Identify the blood parasite species.
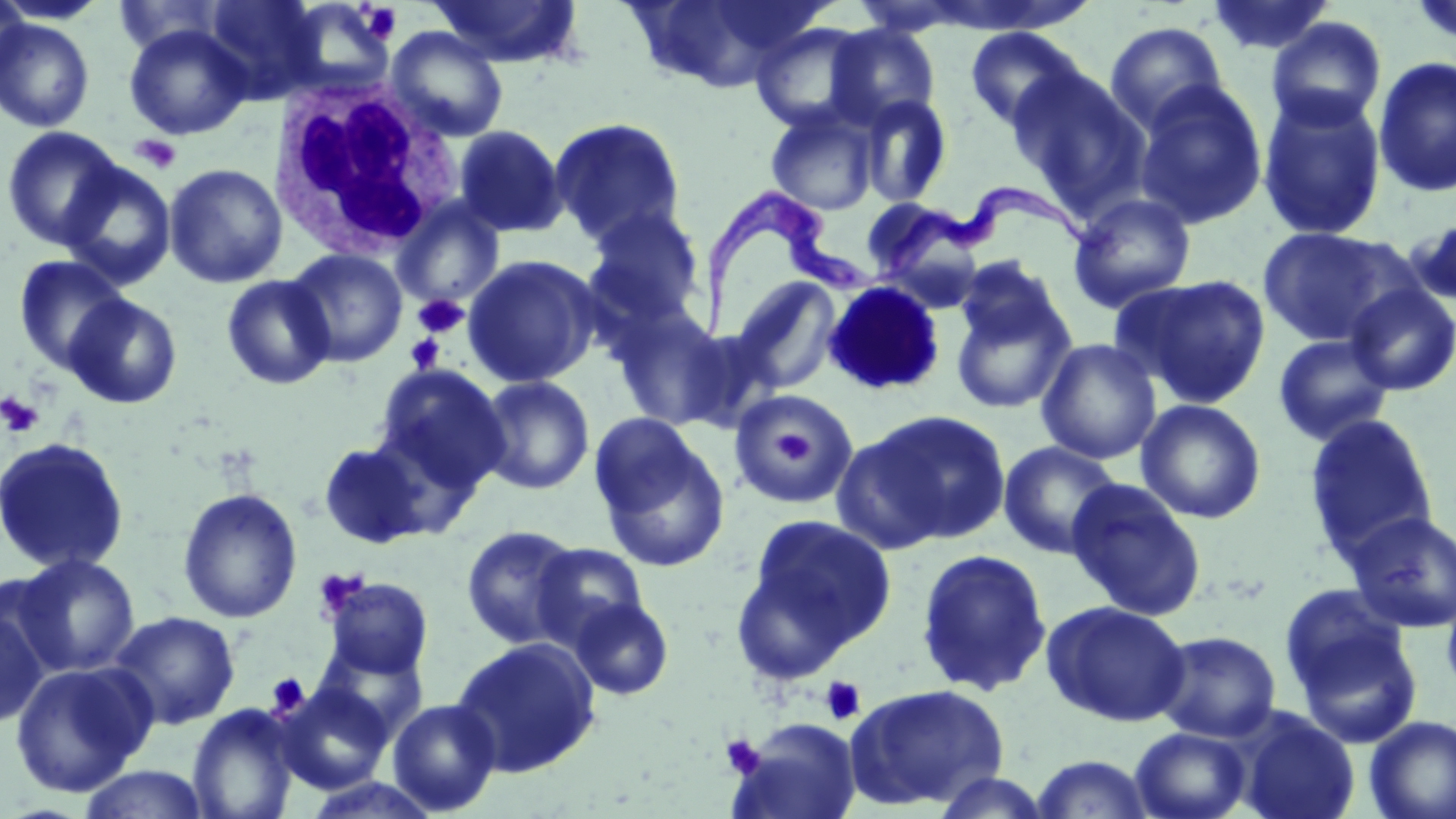

Trypanosoma brucei.

platelet_locations: 'approximate bounding boxes as [x1, y1, x2, y2] in pixels: [360, 3, 403, 44], [130, 134, 182, 174], [413, 294, 468, 338], [404, 333, 446, 375], [0, 391, 45, 438], [763, 414, 827, 479], [266, 673, 309, 716], [820, 676, 866, 726], [721, 734, 765, 778]'
uninfected_red_blood_cell_locations: 'approximate bounding boxes as [x1, y1, x2, y2] in pixels: [0, 0, 30, 90], [0, 0, 110, 26], [114, 0, 228, 58], [203, 0, 326, 102], [429, 0, 584, 68], [1206, 0, 1336, 57], [1408, 0, 1456, 51], [631, 1, 822, 92], [1266, 17, 1387, 132], [0, 18, 95, 133], [749, 21, 875, 133], [1105, 21, 1228, 135], [824, 23, 941, 128], [124, 24, 253, 140], [964, 25, 1090, 132], [386, 26, 510, 143], [1373, 56, 1456, 198], [1006, 66, 1150, 212], [1133, 81, 1269, 229], [857, 93, 953, 208], [1257, 93, 1387, 242], [765, 105, 879, 216], [548, 117, 687, 248], [452, 124, 568, 239], [1, 126, 127, 251], [58, 160, 177, 289], [163, 163, 288, 289], [1067, 192, 1197, 313], [859, 197, 983, 287], [392, 198, 505, 309], [581, 206, 707, 329], [1407, 217, 1456, 306], [1255, 225, 1412, 347], [285, 248, 408, 368], [13, 254, 131, 373], [462, 254, 603, 388], [954, 255, 1068, 357], [1116, 273, 1273, 409], [221, 274, 336, 391], [731, 276, 843, 393], [949, 278, 1077, 415], [1344, 283, 1456, 396], [63, 293, 183, 409], [610, 304, 733, 430], [1272, 333, 1396, 446], [1036, 338, 1162, 464], [373, 364, 511, 496], [477, 375, 595, 495], [729, 390, 859, 508], [1136, 398, 1266, 524], [845, 409, 1011, 548], [1303, 413, 1439, 565], [590, 415, 731, 572], [0, 436, 131, 575], [317, 441, 431, 548], [998, 441, 1123, 559], [1065, 478, 1208, 621], [177, 487, 303, 623], [1346, 511, 1456, 634], [734, 513, 897, 677], [460, 525, 581, 650], [532, 542, 649, 651], [915, 548, 1052, 697], [9, 553, 141, 678], [319, 576, 434, 682], [1440, 580, 1456, 705], [0, 592, 54, 731], [1282, 593, 1421, 744], [568, 597, 675, 701], [1041, 600, 1192, 727], [108, 610, 240, 730], [1152, 630, 1282, 743], [450, 636, 602, 778], [311, 641, 430, 743], [9, 661, 157, 799], [843, 682, 1010, 811], [275, 683, 393, 794], [387, 698, 502, 815], [186, 704, 301, 819], [1235, 710, 1359, 819], [1363, 715, 1456, 819], [730, 718, 864, 819], [1130, 727, 1253, 819], [1028, 754, 1158, 818], [76, 765, 211, 819], [928, 771, 1053, 817], [299, 775, 443, 818]'
stain: May-Grünwald-Giemsa
white_blood_cell_locations: 'approximate bounding boxes as [x1, y1, x2, y2] in pixels: [269, 69, 465, 260]'
trypanosoma_brucei_locations: 'approximate bounding boxes as [x1, y1, x2, y2] in pixels: [872, 182, 1111, 289], [686, 186, 875, 344]'
field_of_view: one of a larger specimen
magnification: 1000x
image_size: 1456×819 pixels
preparation: thin blood film
modality: light microscopy